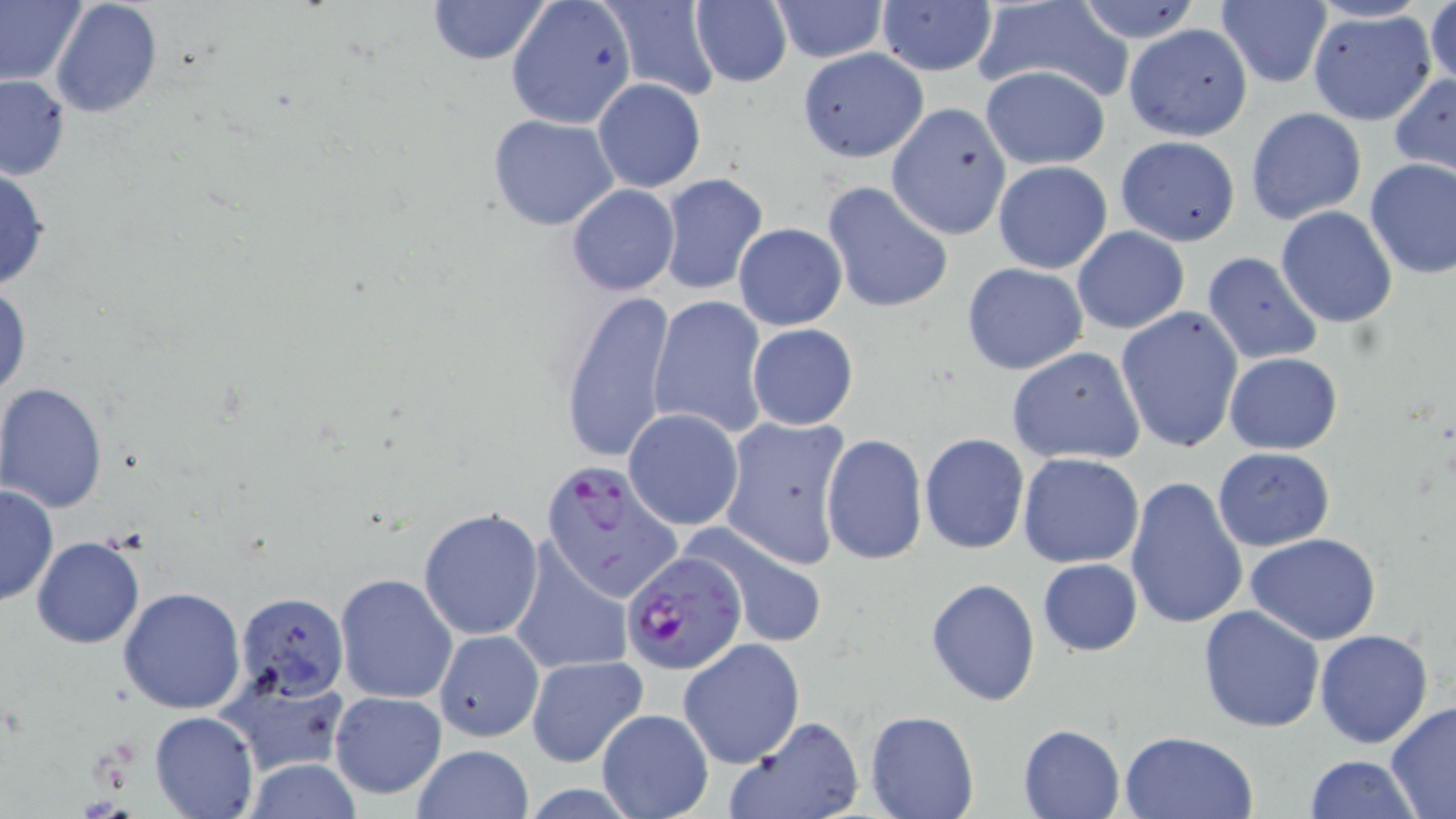
Summary:
  - Coordinate format: approximate bounding boxes as named x1/y1/x2/y2 corners in pixels
  - Uninfected red blood cell locations: (x1=0, y1=0, x2=89, y2=88), (x1=48, y1=0, x2=163, y2=118), (x1=425, y1=0, x2=553, y2=66), (x1=505, y1=0, x2=637, y2=129), (x1=599, y1=0, x2=722, y2=101), (x1=689, y1=0, x2=792, y2=87), (x1=1214, y1=0, x2=1334, y2=88), (x1=769, y1=1, x2=889, y2=64), (x1=1072, y1=1, x2=1206, y2=45), (x1=1427, y1=1, x2=1456, y2=94), (x1=876, y1=2, x2=997, y2=77), (x1=971, y1=2, x2=1133, y2=101), (x1=1306, y1=9, x2=1439, y2=127), (x1=1123, y1=23, x2=1253, y2=141), (x1=796, y1=49, x2=928, y2=163), (x1=980, y1=65, x2=1110, y2=171), (x1=1389, y1=73, x2=1456, y2=178), (x1=0, y1=74, x2=72, y2=182), (x1=592, y1=78, x2=707, y2=192), (x1=886, y1=102, x2=1011, y2=242), (x1=1245, y1=108, x2=1367, y2=226), (x1=486, y1=114, x2=620, y2=230), (x1=1114, y1=135, x2=1241, y2=245), (x1=1364, y1=157, x2=1456, y2=278), (x1=991, y1=159, x2=1113, y2=274), (x1=0, y1=164, x2=52, y2=295), (x1=655, y1=173, x2=767, y2=294), (x1=822, y1=182, x2=951, y2=314), (x1=566, y1=184, x2=679, y2=297), (x1=1276, y1=205, x2=1398, y2=329), (x1=733, y1=223, x2=846, y2=330), (x1=1072, y1=226, x2=1189, y2=335), (x1=1202, y1=251, x2=1324, y2=366), (x1=961, y1=263, x2=1088, y2=375), (x1=0, y1=281, x2=31, y2=405), (x1=555, y1=286, x2=677, y2=465), (x1=648, y1=295, x2=769, y2=438), (x1=1115, y1=306, x2=1243, y2=452), (x1=747, y1=323, x2=858, y2=431), (x1=1006, y1=346, x2=1147, y2=466), (x1=1224, y1=352, x2=1342, y2=454), (x1=0, y1=382, x2=108, y2=512), (x1=624, y1=408, x2=744, y2=531), (x1=720, y1=413, x2=853, y2=568), (x1=820, y1=433, x2=928, y2=566), (x1=920, y1=433, x2=1029, y2=555), (x1=1212, y1=446, x2=1335, y2=551), (x1=1017, y1=452, x2=1144, y2=568), (x1=1124, y1=474, x2=1250, y2=632), (x1=0, y1=484, x2=57, y2=607), (x1=419, y1=509, x2=543, y2=642), (x1=687, y1=523, x2=827, y2=648), (x1=1245, y1=532, x2=1382, y2=645), (x1=31, y1=536, x2=146, y2=648), (x1=507, y1=545, x2=632, y2=679), (x1=1037, y1=557, x2=1142, y2=656), (x1=334, y1=572, x2=458, y2=705), (x1=924, y1=577, x2=1042, y2=707), (x1=118, y1=586, x2=247, y2=714), (x1=235, y1=592, x2=349, y2=697), (x1=1198, y1=604, x2=1325, y2=734), (x1=1315, y1=628, x2=1434, y2=748), (x1=434, y1=630, x2=543, y2=742), (x1=679, y1=638, x2=805, y2=768), (x1=524, y1=654, x2=649, y2=767), (x1=215, y1=668, x2=349, y2=776), (x1=328, y1=690, x2=447, y2=800), (x1=1385, y1=702, x2=1456, y2=818), (x1=596, y1=708, x2=714, y2=819), (x1=865, y1=708, x2=978, y2=819), (x1=150, y1=711, x2=258, y2=819), (x1=723, y1=716, x2=864, y2=819), (x1=1018, y1=724, x2=1125, y2=818), (x1=1118, y1=730, x2=1258, y2=818), (x1=408, y1=744, x2=535, y2=819), (x1=1304, y1=754, x2=1419, y2=819), (x1=242, y1=759, x2=363, y2=817)
  - Plasmodium falciparum-infected red blood cell locations: (x1=535, y1=461, x2=682, y2=619), (x1=619, y1=554, x2=746, y2=676)
  - Slide-level diagnosis: Plasmodium falciparum
  - Preparation: thin blood film
  - Image size: 1456×819 pixels
  - Modality: light microscopy
  - Stain: May-Grünwald-Giemsa
  - Magnification: 1000x
  - Field of view: one of a larger specimen